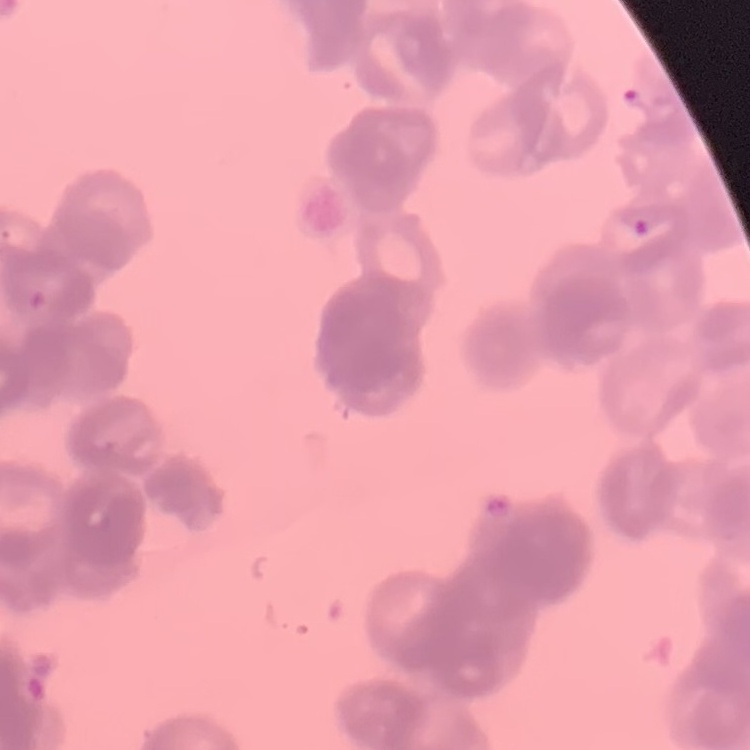
Summary:
  - Erythrocyte morphology: rouleaux formation
  - Preparation: thin blood film
  - Image type: square crop of a larger photomicrograph
  - Stain: Field's or Giemsa